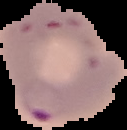

Summary:
  - Image type: cell region segmented out of the field of view; surrounding area masked to black
  - Image size: 127×130 pixels
  - Preparation: thin blood film
  - Result: Plasmodium parasites identified